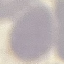
result = no malaria parasites detected
stain = Giemsa
image type = cell patch, automatically extracted from a larger field of view and resized to 64 × 64 pixels
capture = smartphone through the microscope eyepiece
preparation = thin blood smear